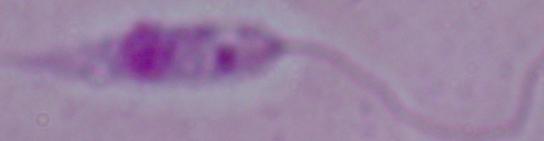

modality = photomicrograph
magnification = 1000x
identification = Leishmania